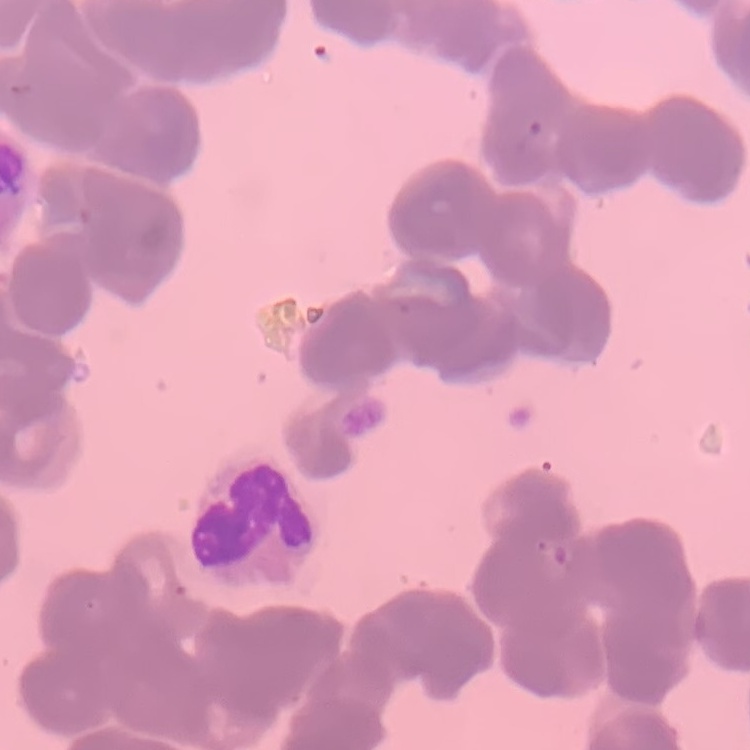

The red blood cells exhibit rouleaux formation. Thin blood smear. One tile cut from a larger photomicrograph. Field's or Giemsa stain.